Assess this cell for malaria.
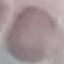
It is uninfected.

Summary:
  - Image type: automatically extracted cell patch, resized to 64 × 64 pixels
  - Capture: smartphone camera at the microscope eyepiece
  - Stain: Giemsa
  - Preparation: thin smear